Assess the morphology of the erythrocytes.
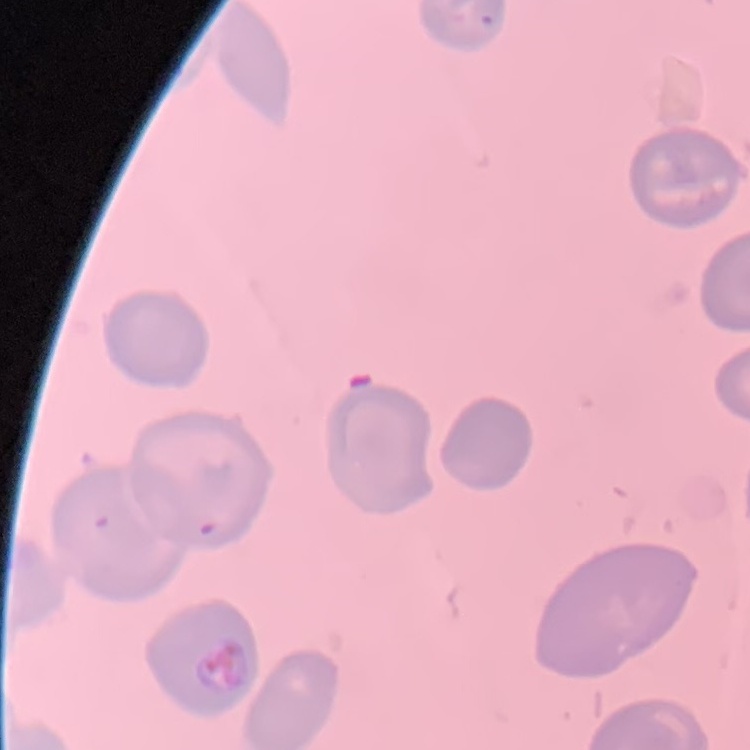

No rouleaux formation.

Summary:
  - Stain: Field's or Giemsa
  - Preparation: thin peripheral smear
  - Image type: one tile cut from a larger photomicrograph